Outline each blood parasite and name the species.
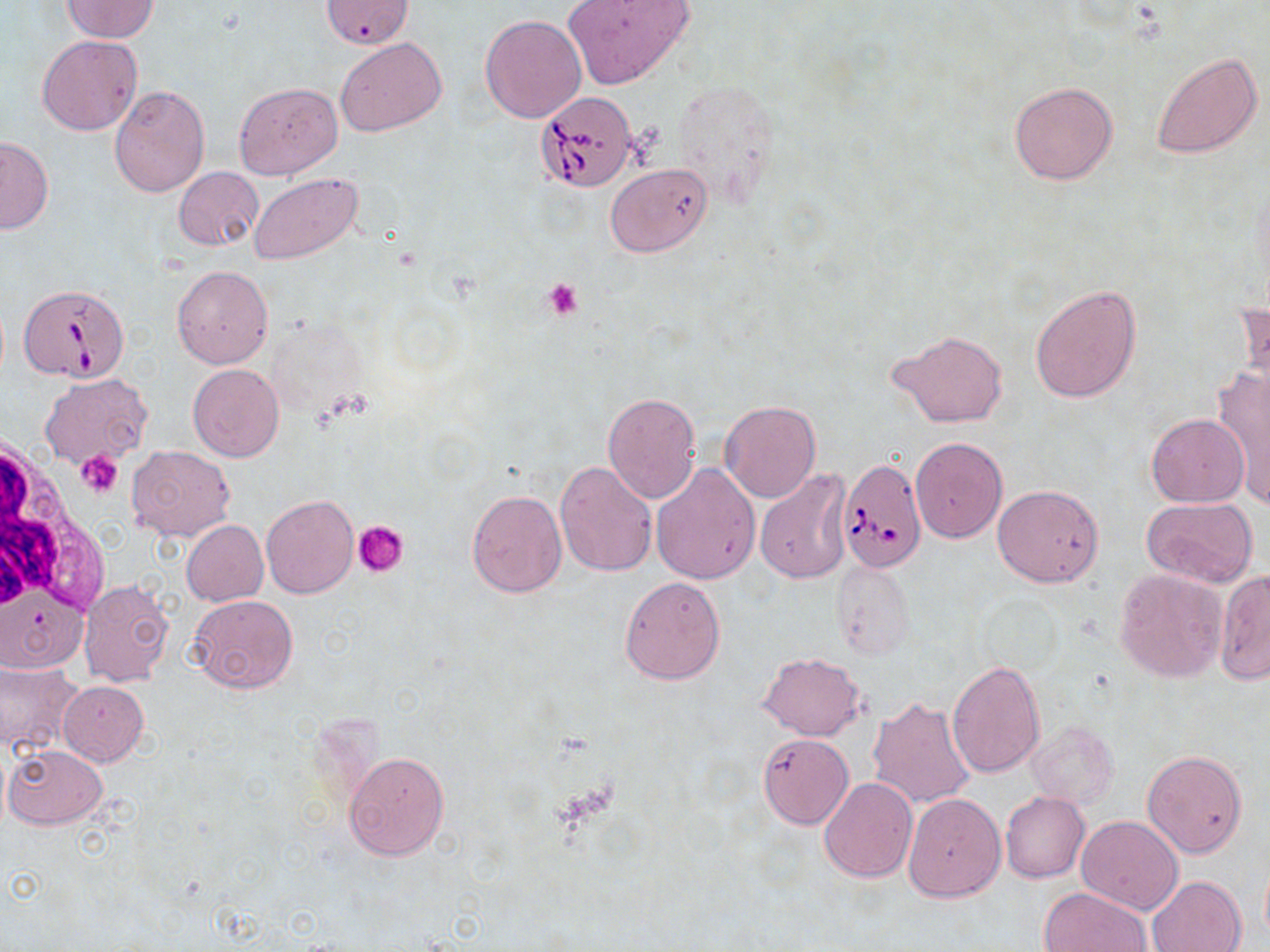
Approximate bounding boxes as (x1, y1, x2, y2) in pixels.
Babesia divergens-infected red blood cells: (535, 91, 638, 191), (18, 284, 128, 384), (838, 458, 926, 573).
No Plasmodium falciparum, Plasmodium ovale, Plasmodium malariae, Plasmodium vivax, or Trypanosoma brucei observed.

slide-level diagnosis = Babesia divergens
preparation = thin blood film
magnification = 1000x
image size = 1270×952 pixels
white blood cell locations = approximate bounding boxes as (x1, y1, x2, y2) in pixels: (0, 432, 105, 634)
platelet locations = approximate bounding boxes as (x1, y1, x2, y2) in pixels: (542, 277, 585, 319), (78, 450, 123, 496), (354, 520, 409, 578)
uninfected red blood cell locations = approximate bounding boxes as (x1, y1, x2, y2) in pixels: (61, 1, 160, 42), (318, 1, 415, 49), (562, 1, 694, 90), (481, 14, 587, 123), (37, 35, 142, 135), (336, 37, 446, 136), (1150, 50, 1262, 159), (669, 76, 782, 208), (1009, 80, 1118, 185), (234, 81, 343, 180), (108, 85, 211, 197), (0, 136, 53, 234), (607, 164, 712, 256), (174, 167, 263, 251), (250, 174, 361, 264), (172, 266, 273, 368), (1030, 284, 1141, 404), (1234, 294, 1270, 403), (887, 331, 1008, 427), (188, 363, 283, 461), (1210, 364, 1270, 506), (40, 372, 151, 467), (603, 392, 700, 502), (721, 400, 820, 502), (1146, 413, 1249, 507), (910, 437, 1007, 541), (128, 445, 236, 540), (555, 460, 658, 576), (651, 464, 760, 584), (755, 468, 853, 584), (993, 484, 1103, 587), (467, 489, 567, 598), (262, 495, 358, 598), (1140, 498, 1258, 588), (181, 519, 269, 606), (831, 561, 915, 657), (1113, 568, 1227, 682), (1215, 570, 1270, 684), (620, 576, 726, 684), (78, 579, 173, 686), (188, 594, 298, 696), (758, 652, 866, 742), (0, 660, 82, 755), (947, 660, 1045, 779), (58, 681, 148, 765), (869, 696, 975, 810), (1028, 721, 1118, 808), (757, 732, 854, 830), (3, 745, 107, 829), (343, 749, 450, 860), (1141, 750, 1249, 859), (818, 777, 917, 883), (903, 792, 1005, 901), (1000, 792, 1089, 883), (1076, 816, 1185, 914), (1148, 875, 1247, 952), (1040, 887, 1152, 952)
stain = May-Grünwald-Giemsa
modality = light microscopy
field of view = one of a larger specimen